Report the malaria status of this cell.
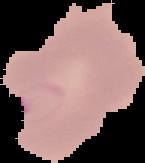

It is parasitized.

Image is 145×163 pixels. From a thin blood smear. The area outside the segmented cell region is set to black.